State the blood parasite species.
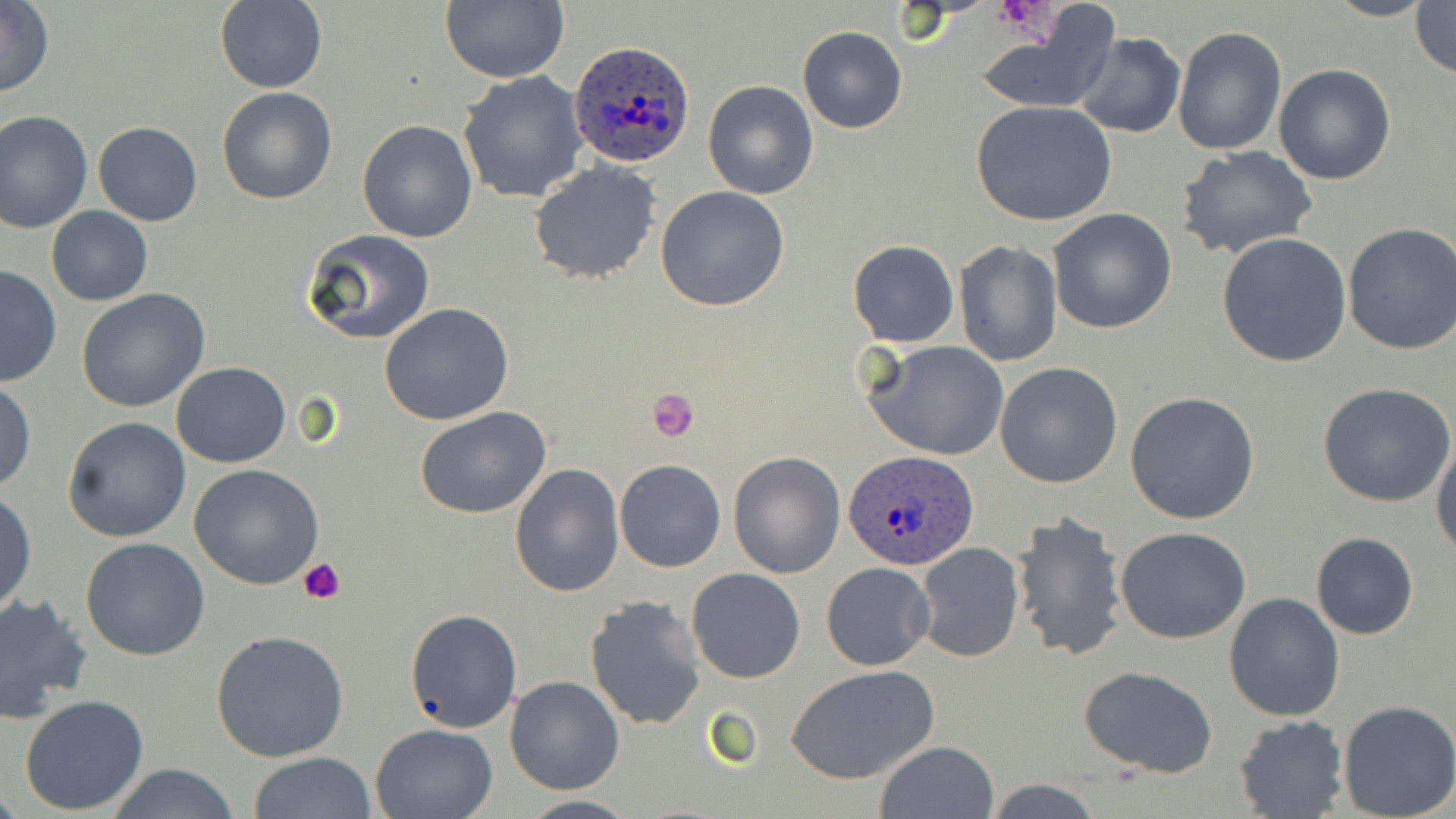
Plasmodium ovale.

Summary:
  - Coordinate format: approximate bounding boxes as (x1,y1)-(x2,y2) corner pairs in pixels
  - Plasmodium ovale-infected red blood cell locations: (569,42)-(696,169), (844,449)-(978,571)
  - Platelet locations: (995,0)-(1053,34), (646,387)-(699,442), (300,559)-(348,605)
  - Uninfected red blood cell locations: (439,0)-(567,83), (1323,0)-(1436,21), (1,1)-(54,98), (215,1)-(327,92), (1410,1)-(1455,78), (973,15)-(1117,113), (798,27)-(907,132), (1172,27)-(1286,156), (1072,32)-(1186,139), (1274,63)-(1395,185), (458,72)-(588,204), (702,81)-(818,200), (216,86)-(338,205), (971,101)-(1116,227), (0,108)-(94,234), (356,119)-(478,242), (92,121)-(202,226), (1174,145)-(1318,260), (529,161)-(660,284), (656,186)-(789,312), (46,206)-(152,306), (1048,207)-(1179,334), (1341,223)-(1456,357), (304,229)-(435,344), (1216,231)-(1354,367), (848,238)-(958,348), (954,242)-(1062,366), (0,264)-(61,389), (76,290)-(209,412), (379,303)-(512,425), (862,340)-(1010,460), (171,361)-(290,467), (995,362)-(1124,488), (0,380)-(37,492), (1318,382)-(1454,507), (1124,391)-(1260,525), (414,407)-(552,517), (62,417)-(191,542), (1431,439)-(1456,558), (727,452)-(845,578), (614,458)-(725,572), (511,461)-(625,596), (189,464)-(324,589), (0,488)-(37,615), (1009,509)-(1128,661), (1117,527)-(1251,643), (1310,533)-(1419,639), (80,537)-(211,660), (913,542)-(1025,663), (821,562)-(935,670), (686,568)-(806,683), (1224,593)-(1344,721), (0,594)-(93,722), (585,595)-(709,732), (405,608)-(522,733), (210,630)-(350,762), (788,666)-(940,785), (1079,666)-(1216,778), (504,676)-(624,794), (19,694)-(150,813), (1337,700)-(1456,818), (1233,715)-(1347,818), (369,723)-(498,819), (876,741)-(998,818), (249,752)-(376,819), (104,763)-(242,819), (984,779)-(1103,818), (513,794)-(640,818)
  - Preparation: thin blood film
  - Modality: light microscopy
  - Field of view: one of a larger specimen
  - Image size: 1456×819 pixels
  - Stain: May-Grünwald-Giemsa
  - Magnification: 1000x